Outline each uninfected red blood cell.
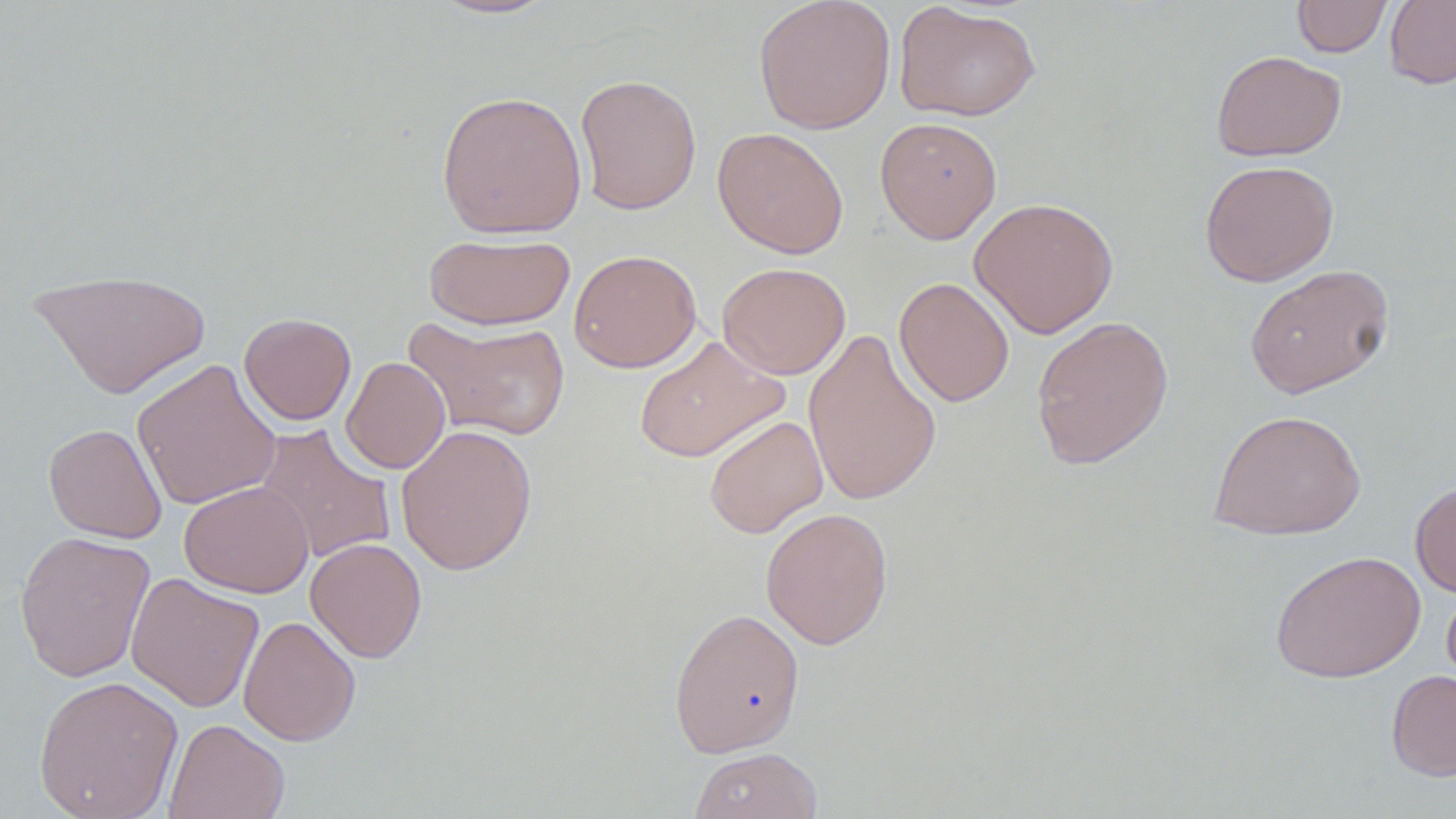

Approximate bounding boxes as (x1, y1, x2, y2) in pixels.
Uninfected red blood cells: (430, 0, 562, 21), (752, 0, 896, 135), (1292, 0, 1392, 57), (1385, 0, 1456, 89), (894, 2, 1041, 121), (1211, 50, 1346, 162), (574, 73, 702, 215), (436, 89, 587, 239), (874, 117, 1002, 244), (712, 126, 849, 259), (1199, 159, 1339, 286), (968, 196, 1120, 339), (423, 232, 575, 330), (568, 249, 703, 373), (717, 261, 851, 379), (1244, 263, 1394, 399), (29, 268, 213, 399), (894, 276, 1014, 407), (239, 312, 356, 425), (1031, 315, 1174, 469), (405, 317, 572, 442), (803, 327, 942, 507), (634, 335, 789, 463), (341, 356, 450, 474), (131, 358, 282, 511), (1209, 408, 1366, 540), (703, 414, 828, 538), (43, 423, 167, 544), (254, 424, 397, 565), (395, 424, 538, 575), (1410, 479, 1456, 597), (179, 481, 314, 598), (760, 507, 893, 649), (14, 530, 156, 683), (305, 537, 428, 663), (1270, 549, 1425, 683), (126, 571, 265, 713), (1441, 583, 1456, 695), (668, 607, 806, 758), (238, 615, 361, 746), (1386, 669, 1456, 781), (33, 675, 184, 819), (164, 718, 289, 819), (689, 746, 822, 819).

Summary:
  - Slide-level diagnosis: negative for blood parasites
  - Modality: optical microscopy
  - Image size: 1456×819 pixels
  - Preparation: thin blood smear
  - Stain: May-Grünwald-Giemsa
  - Field of view: one of a larger specimen
  - Magnification: 1000x